Assess the morphology of the erythrocytes.
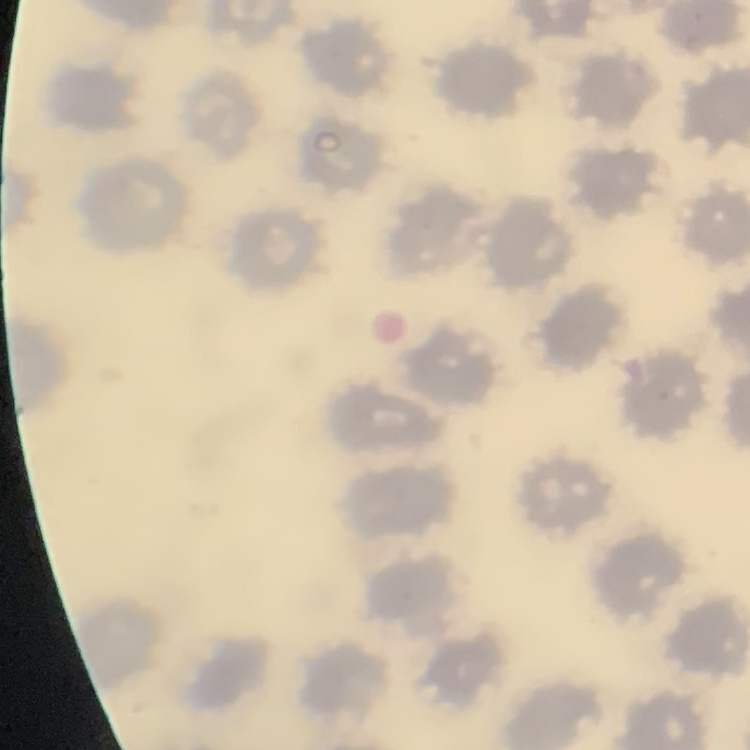
They show no rouleaux formation.

Summary:
  - Preparation: thin blood film
  - Stain: Field's or Giemsa
  - Image type: square crop of a larger photomicrograph